State which parasite is depicted.
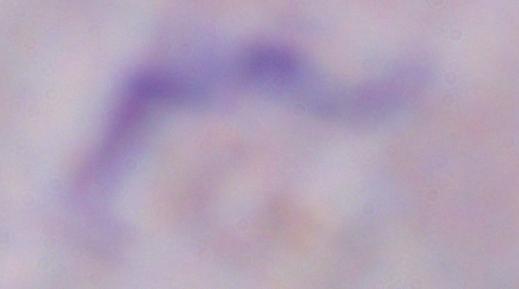
A trypanosome.

Captured at 1000x magnification. Micrograph.